Name the cell type shown.
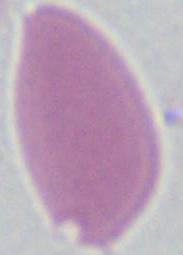

This is an erythrocyte.

magnification = 1000x
modality = micrograph